Identify the parasite.
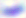
Toxoplasma gondii.

{
  "modality": "photomicrograph",
  "magnification": "400x"
}